Identify the preparation type.
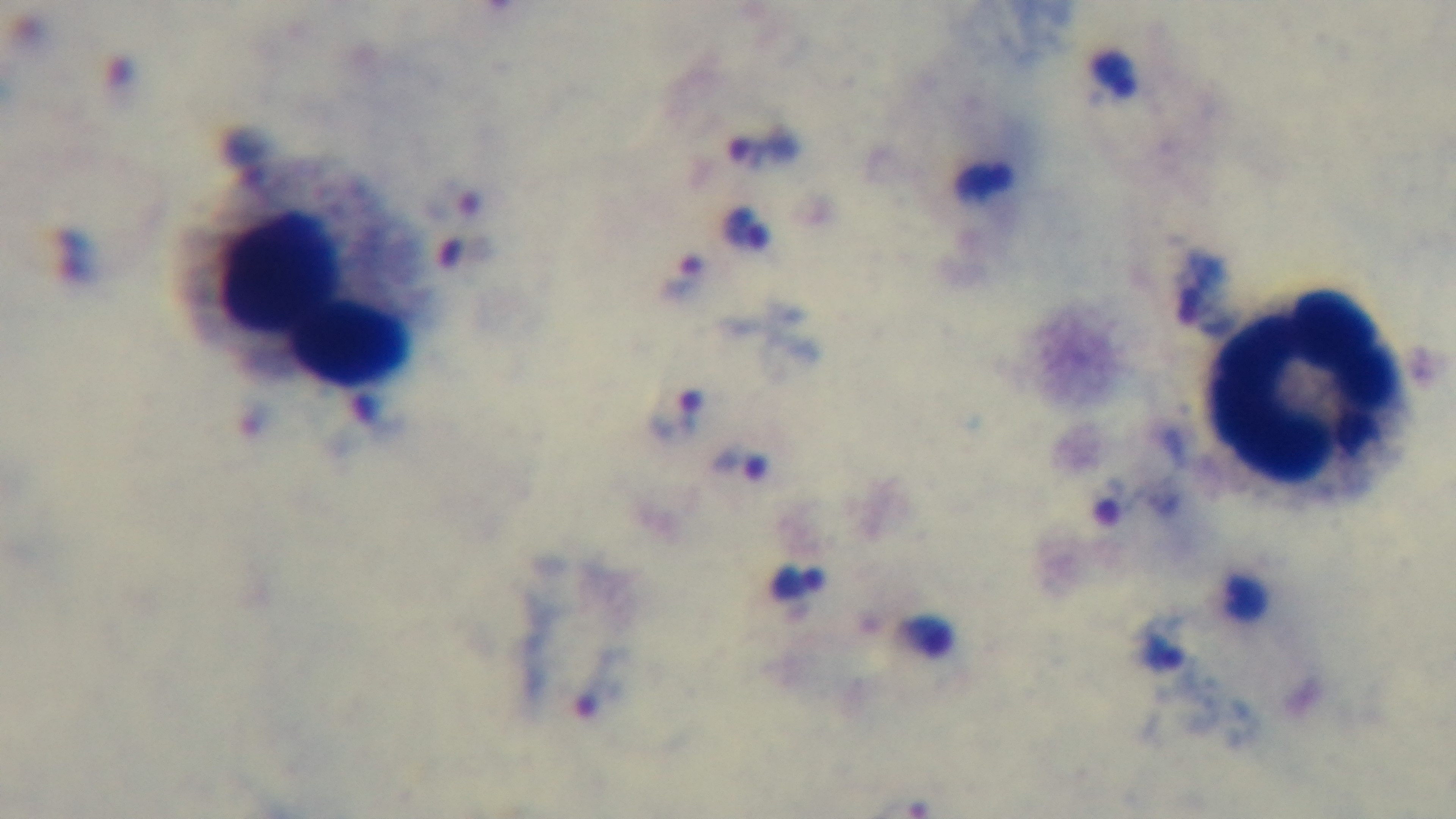

A thick smear.

Captured with a mounted 4K digital camera. One field from the slide. Malaria status: positive. 100x oil-immersion objective. Photomicrograph. Giemsa-stained.